Report the malaria status of this cell.
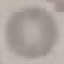

Uninfected.

preparation = thin blood film
capture = smartphone camera at the microscope eyepiece
image type = automatically extracted cell patch, resized to 64 × 64 pixels
stain = Giemsa